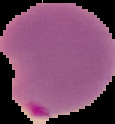 Cell region segmented out of the field of view; the surrounding area is masked to black. Malaria status: parasitized. From a thin blood smear. Image is 115×124 pixels.